Point out each malaria parasite.
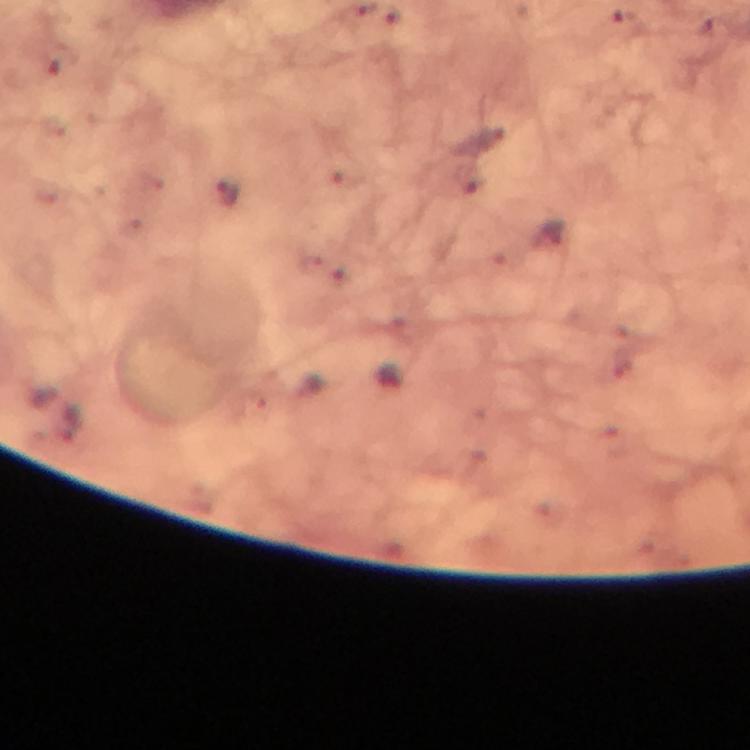

Approximate centers as {x, y} in pixels.
Malaria parasites: {394, 13}, {627, 25}, {490, 135}, {473, 181}, {226, 193}, {552, 233}, {68, 425}.

Summary:
  - Capture: smartphone mounted on the microscope
  - Cropped from: one field of view
  - Stain: Giemsa
  - Preparation: thick blood film
  - Immersion oil: used
  - Image size: 750×750 pixels
  - Context: from a malaria diagnostic workup
  - Magnification: 100x